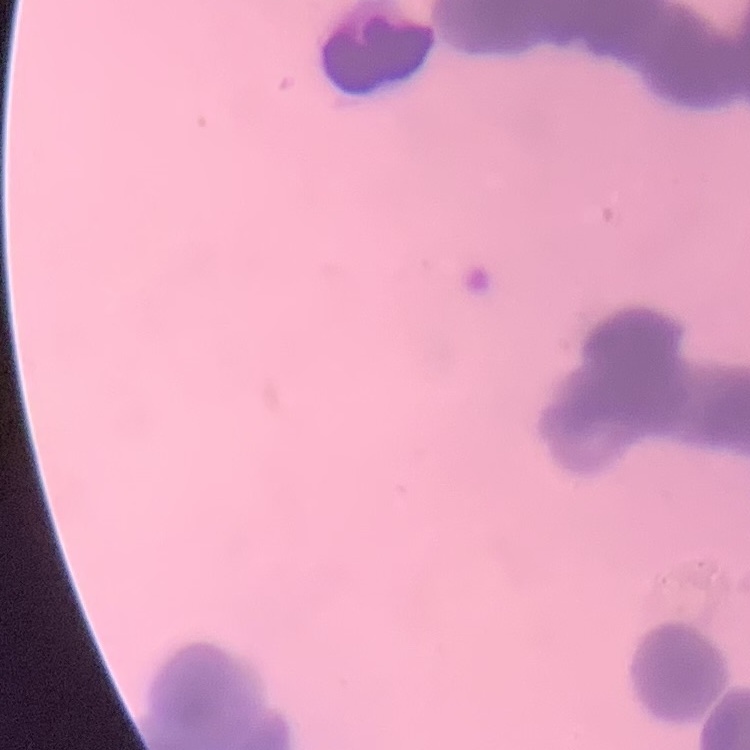

Summary:
  - Red blood cell morphology: rouleaux formation
  - Preparation: thin blood film
  - Stain: Field's or Giemsa
  - Image type: one tile cut from a larger photomicrograph